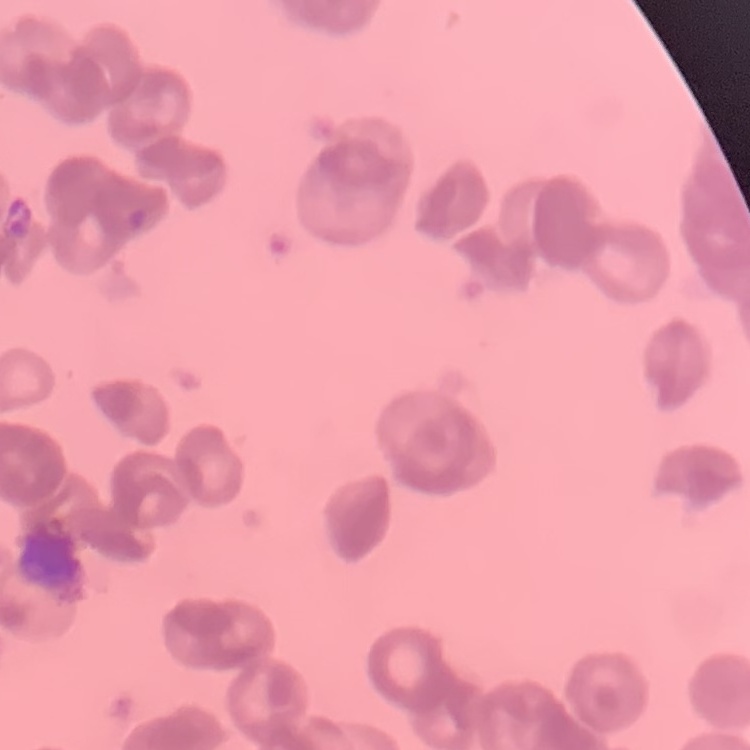 The erythrocytes exhibit rouleaux formation. Field's or Giemsa stain. Thin peripheral smear. One tile cut from a larger photomicrograph.